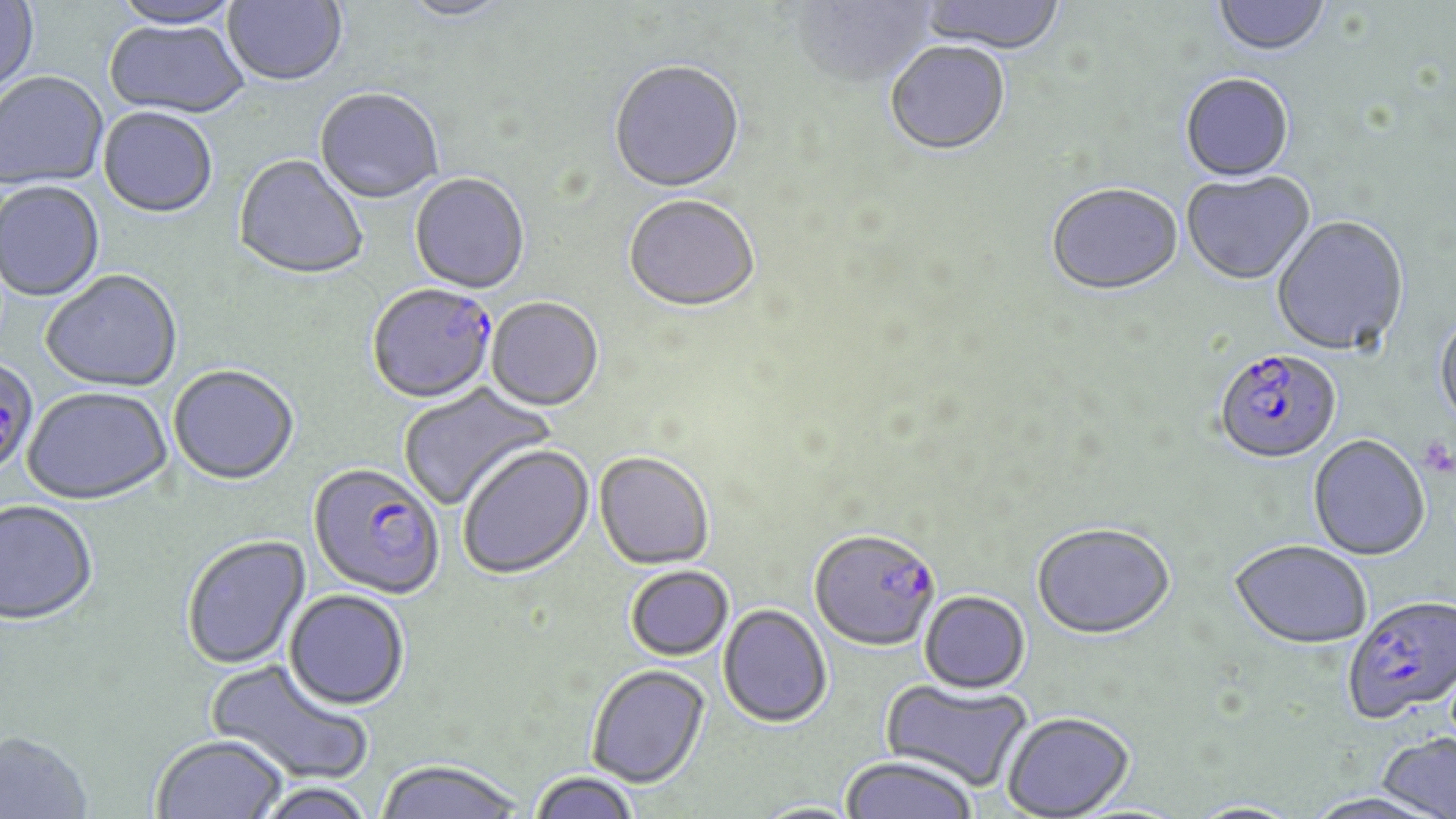
Approximate bounding boxes as (x1,y1)-(x2,y2) corner pairs in pixels. Uninfected red blood cell locations: (111,0)-(244,30), (223,0)-(348,89), (396,0)-(517,24), (792,0)-(937,91), (918,0)-(1066,57), (1213,0)-(1330,59), (0,1)-(40,103), (104,21)-(249,120), (885,44)-(1010,158), (608,63)-(746,196), (1,73)-(109,193), (1180,76)-(1295,184), (314,90)-(443,206), (97,109)-(217,221), (233,156)-(369,283), (1182,172)-(1316,287), (409,175)-(530,296), (0,182)-(105,303), (1046,186)-(1184,299), (623,197)-(761,315), (1272,216)-(1409,358), (41,271)-(183,394), (486,299)-(604,413), (1434,312)-(1456,431), (168,367)-(299,488), (398,380)-(557,511), (21,389)-(173,508), (1308,435)-(1430,560), (458,445)-(594,580), (594,452)-(715,571), (0,501)-(98,628), (1032,522)-(1174,639), (182,535)-(312,671), (1230,539)-(1372,648), (625,565)-(734,661), (283,590)-(410,712), (920,591)-(1030,693), (718,604)-(832,728), (205,658)-(375,788), (586,663)-(710,788), (880,677)-(1034,792), (1001,711)-(1134,818), (0,730)-(94,819), (1376,732)-(1456,819), (151,736)-(287,819), (840,756)-(978,818), (374,759)-(526,819), (530,772)-(640,819), (250,782)-(377,819), (1301,791)-(1448,818), (751,800)-(866,819), (1188,800)-(1306,818). Plasmodium falciparum-infected red blood cell locations: (367,285)-(498,406), (1214,350)-(1342,466), (0,358)-(39,478), (307,463)-(446,601), (809,529)-(941,653), (1343,593)-(1456,723). Platelet locations: (1419,435)-(1455,477). Slide-level diagnosis: Plasmodium falciparum. Light microscopy. May-Grünwald-Giemsa-stained preparation. Thin blood film. One field of a larger specimen. Captured at 1000x magnification. Image is 1456×819 pixels.